Comment on the morphology of the red blood cells.
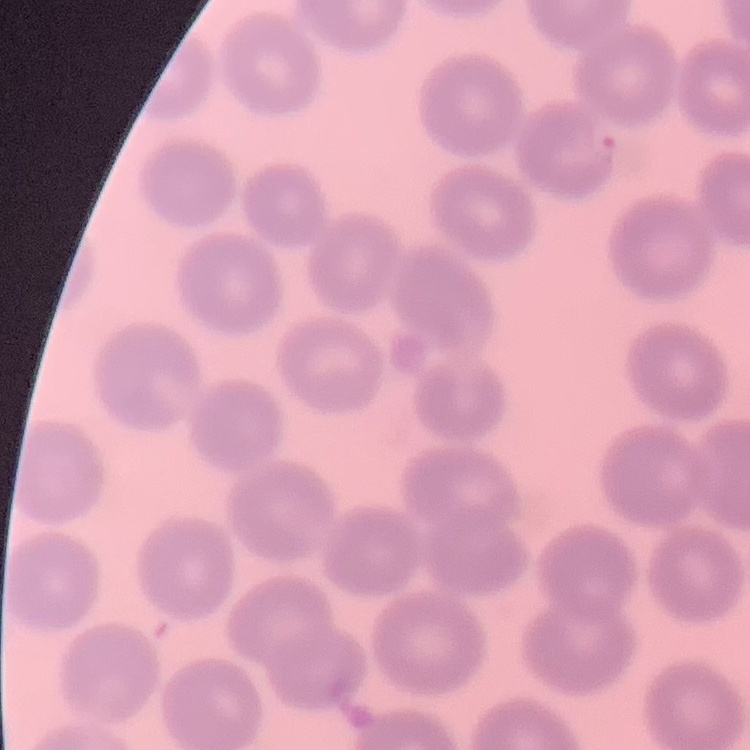

They show no rouleaux formation.

Field's or Giemsa stain. Thin blood smear. Square crop of a larger photomicrograph.